Outline each Plasmodium ovale-infected red blood cell.
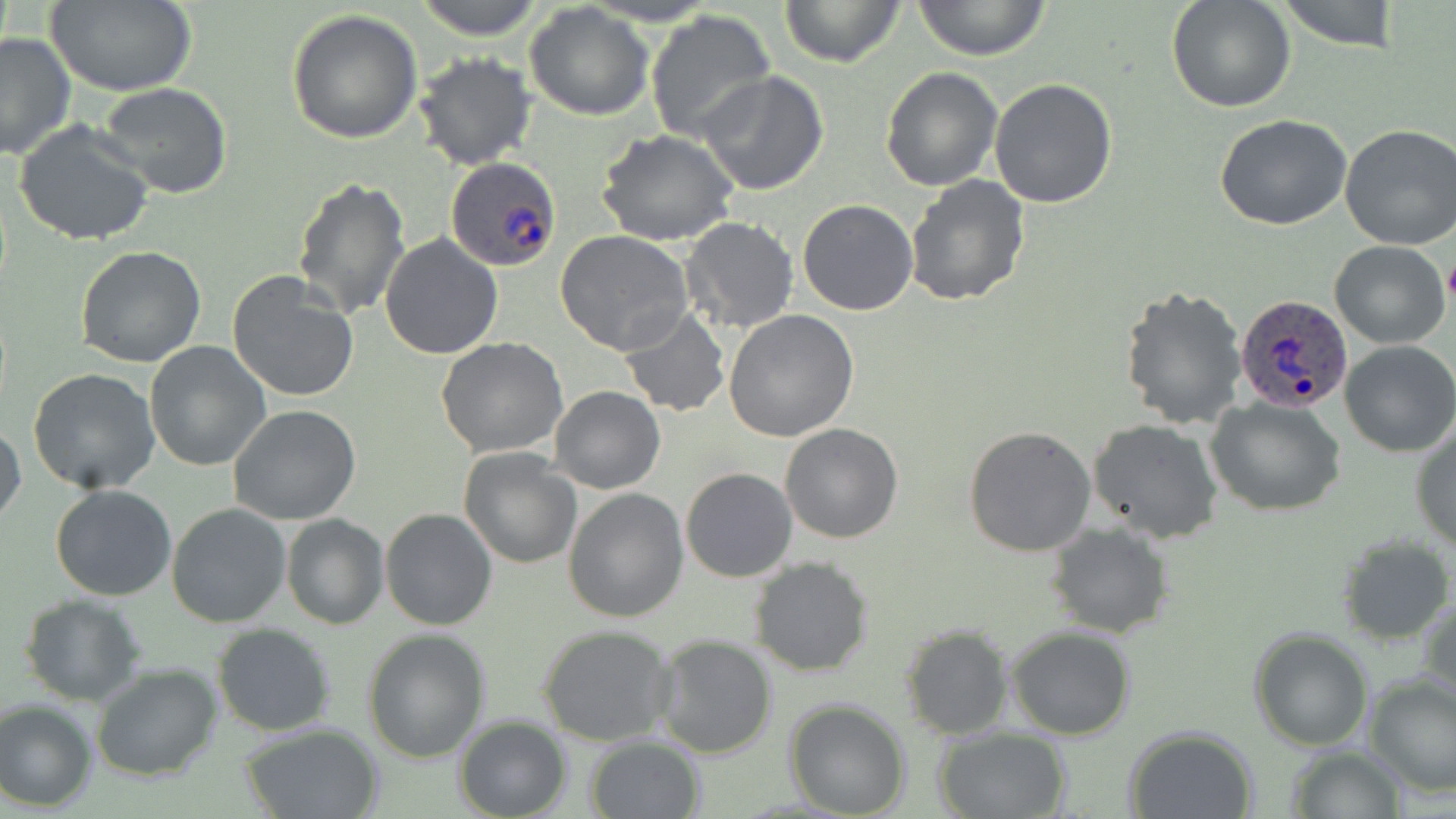
Approximate bounding boxes as (x1, y1, x2, y2) in pixels.
Plasmodium ovale-infected red blood cells: (446, 156, 561, 273), (1235, 293, 1354, 414).

Uninfected red blood cell locations: (413, 0, 547, 41), (777, 0, 908, 71), (912, 0, 1053, 61), (1166, 0, 1296, 112), (1276, 0, 1402, 52), (44, 1, 197, 95), (523, 4, 654, 120), (285, 8, 422, 145), (646, 8, 776, 144), (0, 32, 75, 159), (414, 53, 538, 171), (880, 66, 1002, 191), (697, 71, 829, 196), (989, 79, 1118, 209), (98, 82, 233, 200), (1213, 114, 1353, 230), (15, 120, 155, 247), (1337, 124, 1456, 249), (595, 128, 740, 246), (904, 174, 1033, 307), (291, 176, 412, 320), (797, 199, 921, 316), (680, 216, 799, 335), (555, 230, 696, 357), (380, 231, 504, 358), (1330, 240, 1449, 348), (73, 246, 208, 368), (227, 270, 360, 403), (1119, 284, 1248, 429), (619, 307, 732, 417), (724, 311, 859, 443), (436, 337, 569, 458), (1340, 340, 1456, 457), (144, 341, 271, 471), (27, 369, 160, 495), (551, 385, 665, 493), (1207, 396, 1348, 516), (228, 404, 361, 526), (1085, 417, 1224, 544), (1, 420, 25, 528), (1411, 422, 1456, 554), (780, 423, 903, 544), (964, 425, 1096, 558), (458, 447, 582, 570), (680, 467, 797, 582), (50, 485, 178, 601), (563, 488, 690, 623), (165, 502, 292, 628), (379, 508, 498, 630), (281, 513, 387, 629), (1047, 522, 1174, 639), (1337, 537, 1453, 643), (750, 556, 874, 677), (1418, 593, 1456, 717), (20, 594, 147, 707), (212, 623, 337, 735), (900, 624, 1013, 740), (535, 625, 677, 747), (1007, 626, 1136, 740), (361, 628, 492, 763), (1249, 628, 1373, 750), (653, 635, 778, 758), (1289, 643, 1447, 777), (91, 663, 223, 783), (1364, 675, 1456, 796), (784, 698, 912, 818), (0, 699, 96, 811), (454, 716, 572, 819), (239, 724, 384, 819), (1123, 726, 1258, 818), (933, 727, 1070, 818), (585, 735, 706, 818), (1283, 746, 1407, 819). Platelet locations: (1442, 253, 1456, 309). Slide-level diagnosis: Plasmodium ovale. One field of a larger specimen. Image is 1456×819 pixels. Captured at 1000x magnification. May-Grünwald-Giemsa-stained preparation. Thin blood film. Optical microscopy.